Name the parasite shown.
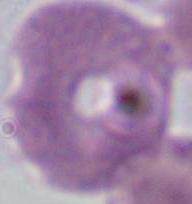
This is Plasmodium.

Micrograph. Captured at either 400x or 1000x magnification.